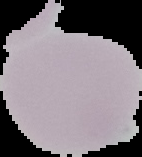

Result: no Plasmodium parasites seen. From a thin blood film. The area outside the segmented cell region is set to black. Image is 142×157 pixels.